Report the malaria status of this cell.
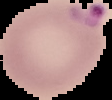
Parasitized.

{
  "image_type": "cell region segmented out of the field of view; surrounding area masked to black",
  "preparation": "thin blood smear",
  "image_size": "112×100 pixels"
}